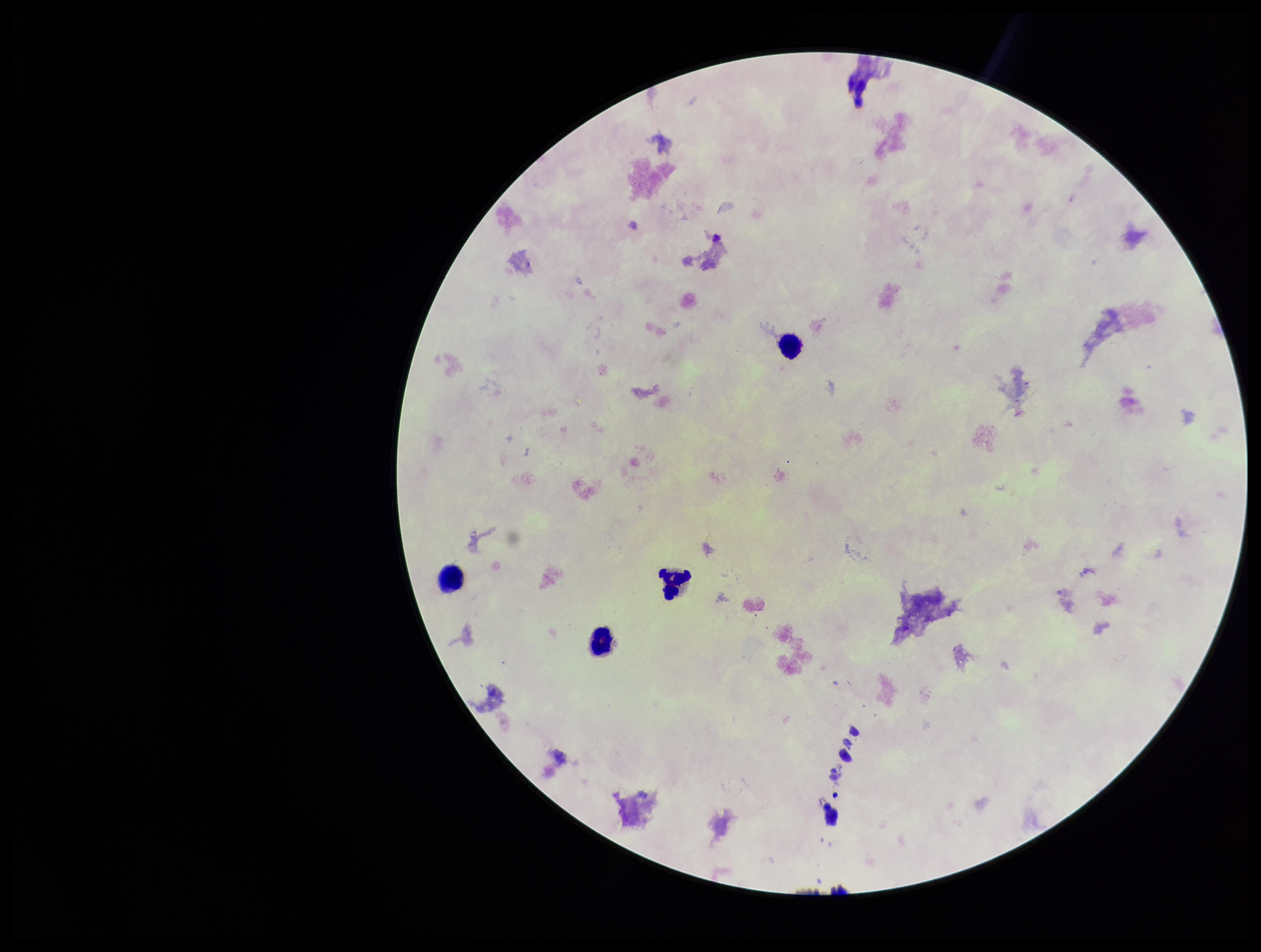

image size = 1261×952 pixels
stain = Giemsa
leukocyte count = 4
patient malaria status = negative
Plasmodium parasites = none detected
preparation = thick
field of view = one from this slide
parasite count = 0
capture = smartphone photograph through the microscope eyepiece